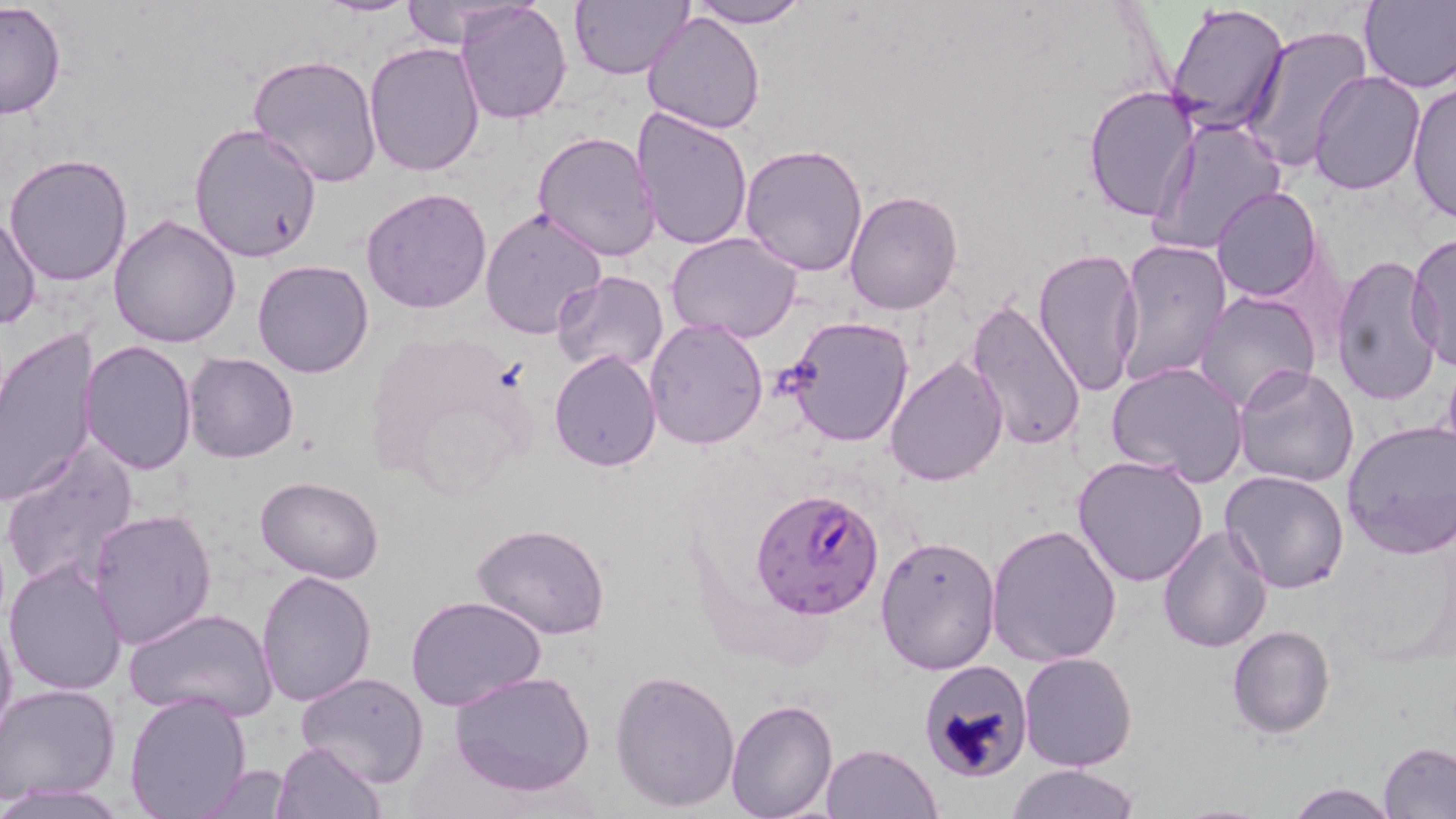

slide_level_diagnosis: Plasmodium falciparum
field_of_view: one of a larger specimen
magnification: 1000x
image_size: 1456×819 pixels
uninfected_red_blood_cell_locations: 'approximate bounding boxes as (x1,y1)-(x2,y2) corner pairs in pixels: (317,0)-(423,16), (396,0)-(527,48), (570,0)-(692,80), (690,0)-(807,28), (1359,0)-(1456,91), (0,1)-(67,121), (457,1)-(572,124), (1165,2)-(1291,138), (643,9)-(765,134), (1239,25)-(1374,173), (364,42)-(486,178), (246,54)-(381,189), (1309,71)-(1425,196), (1405,80)-(1456,225), (1082,85)-(1198,222), (630,106)-(755,252), (1145,115)-(1287,257), (189,124)-(324,262), (531,130)-(662,263), (739,142)-(868,277), (3,153)-(134,287), (1211,185)-(1324,301), (361,188)-(493,313), (844,190)-(963,313), (478,208)-(608,341), (1,210)-(42,331), (108,213)-(241,348), (666,231)-(805,346), (1407,234)-(1455,373), (1114,238)-(1233,386), (1032,247)-(1144,397), (1330,253)-(1444,407), (252,259)-(374,379), (553,272)-(669,375), (1194,289)-(1323,411), (967,299)-(1088,453), (784,315)-(915,447), (645,317)-(768,451), (359,327)-(534,498), (0,330)-(98,506), (81,340)-(197,473), (549,349)-(662,472), (183,352)-(298,462), (883,353)-(1007,487), (1106,362)-(1249,485), (1233,365)-(1360,489), (1342,420)-(1456,558), (1,439)-(139,594), (1073,455)-(1208,588), (1221,470)-(1349,593), (254,476)-(384,584), (87,509)-(217,649), (1156,522)-(1274,651), (985,523)-(1122,669), (472,525)-(611,641), (874,534)-(1001,675), (4,558)-(128,695), (255,570)-(376,706), (407,596)-(549,713), (123,607)-(277,721), (0,608)-(17,751), (1226,624)-(1334,737), (1018,651)-(1139,771), (918,658)-(1033,783), (449,670)-(595,796), (610,670)-(740,812), (295,672)-(430,788), (0,683)-(120,806), (124,691)-(253,819), (725,699)-(838,819), (273,740)-(385,818), (820,742)-(942,819), (1379,743)-(1456,818), (194,763)-(296,817), (1006,763)-(1140,819), (1282,781)-(1402,818)'
stain: May-Grünwald-Giemsa
preparation: thin blood smear
plasmodium_falciparum_infected_red_blood_cell_locations: 'approximate bounding boxes as (x1,y1)-(x2,y2) corner pairs in pixels: (751,487)-(882,616)'
modality: light microscopy